Locate every leukocyte (white blood cell).
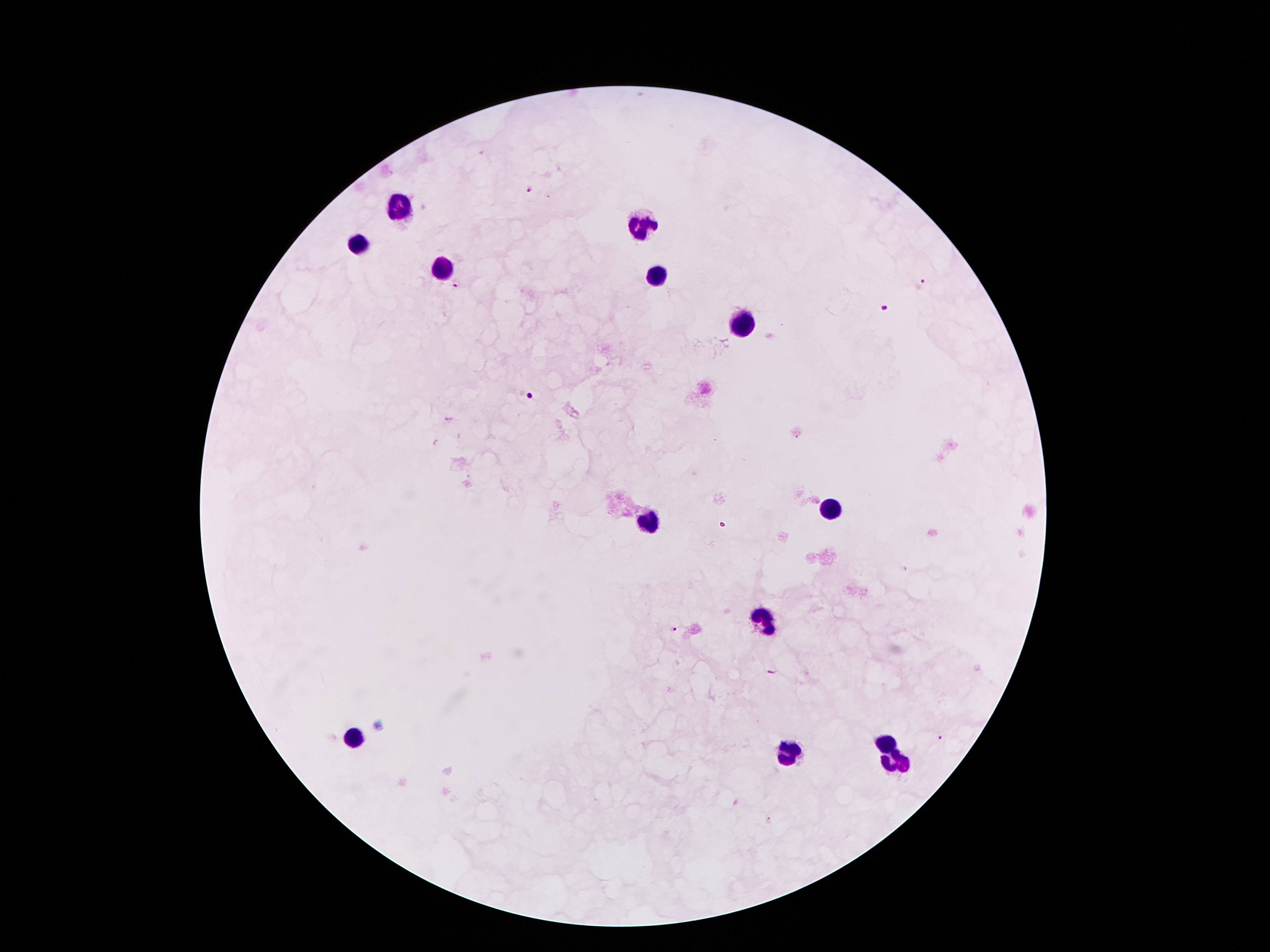

Approximate centers as (x, y) in pixels.
Leukocytes: (401, 209), (641, 227), (360, 243), (439, 270), (655, 277), (741, 329), (834, 511), (650, 525), (764, 618), (357, 738), (886, 747), (789, 754), (897, 764).

Plasmodium parasite locations = (530, 189), (458, 284), (924, 285), (884, 310), (530, 396), (673, 630), (770, 672), (942, 740)
stain = Giemsa
magnification = 100x
field of view = single
patient malaria status = infected with Plasmodium falciparum
preparation = thick peripheral-blood smear
image size = 1270×952 pixels
capture = smartphone camera through the microscope eyepiece